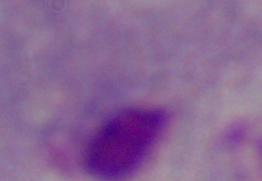

modality = micrograph
magnification = 1000x
identification = trichomonad